Report the malaria status of this cell.
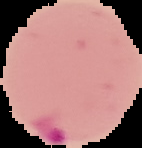
Parasitized.

From a thin blood smear. Image is 142×148 pixels. Cell region segmented out of the field of view; the surrounding area is masked to black.